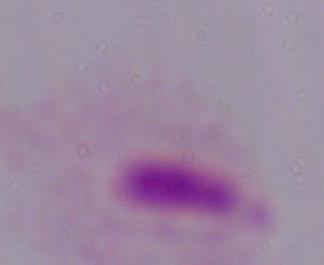
Summary:
  - Identification: trichomonad
  - Modality: micrograph
  - Magnification: 1000x